Assess the morphology of the erythrocytes.
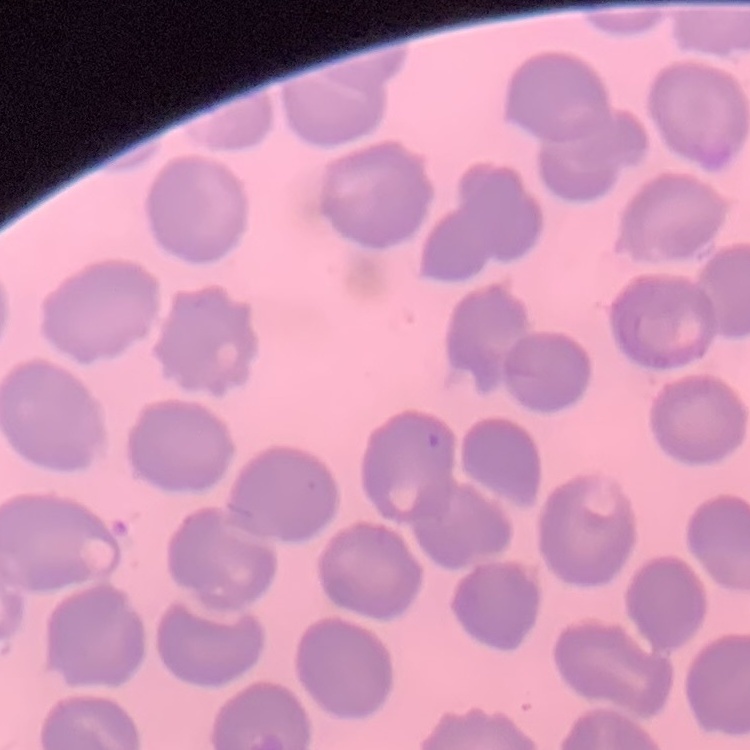

They show no rouleaux formation.

stain: Field's or Giemsa
image_type: one tile cut from a larger photomicrograph
preparation: thin blood smear